Name the blood parasite species.
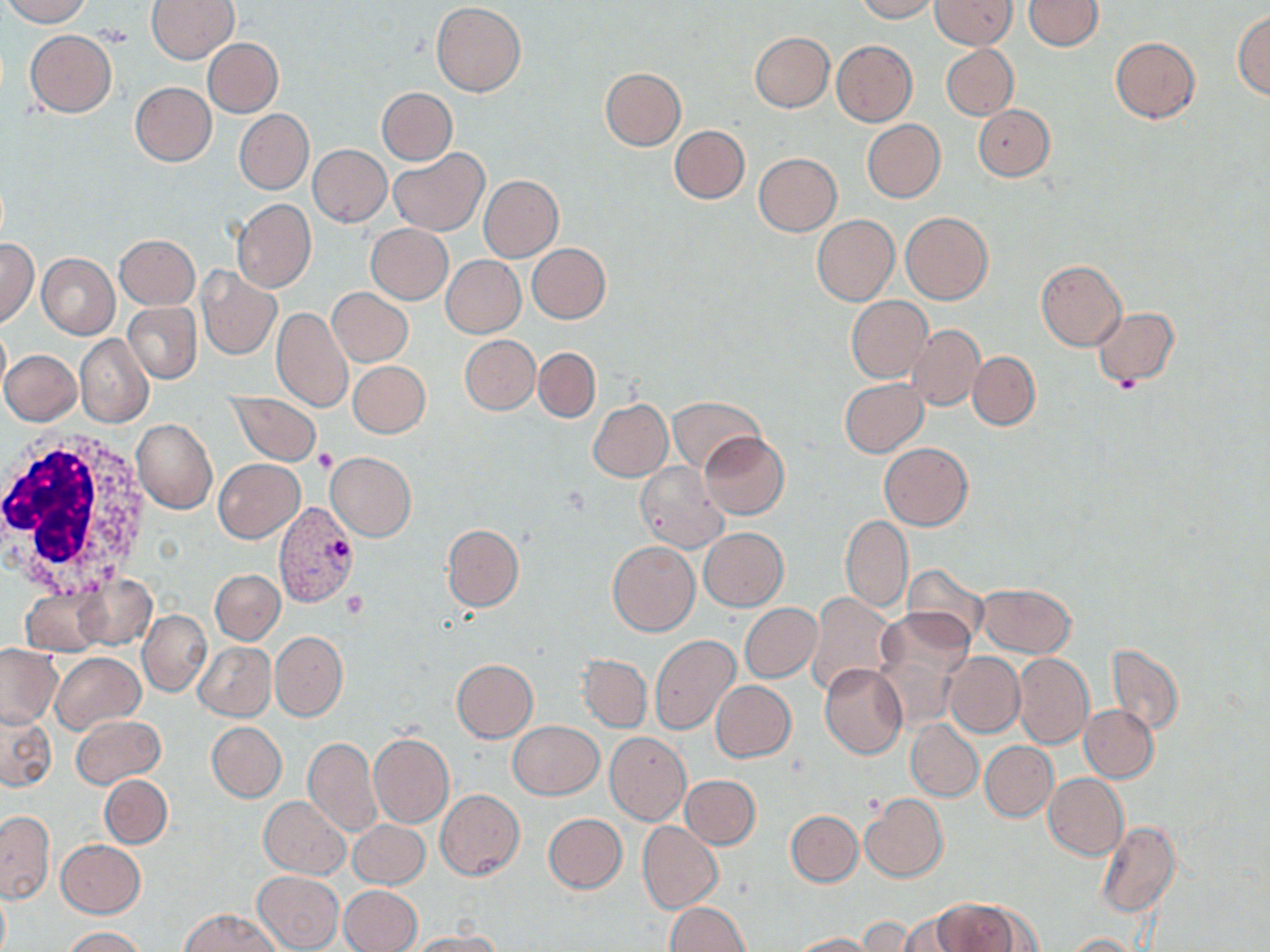

Plasmodium vivax.

Approximate bounding boxes as named x1/y1/x2/y2 corners in pixels. Platelet locations: (x1=312, y1=449, x2=337, y2=473), (x1=342, y1=590, x2=367, y2=620). Plasmodium vivax-infected red blood cell locations: (x1=273, y1=501, x2=356, y2=608). White blood cell locations: (x1=0, y1=428, x2=157, y2=598). Uninfected red blood cell locations: (x1=1, y1=0, x2=92, y2=26), (x1=147, y1=0, x2=239, y2=64), (x1=854, y1=0, x2=937, y2=22), (x1=930, y1=0, x2=1015, y2=49), (x1=1024, y1=0, x2=1104, y2=51), (x1=432, y1=2, x2=525, y2=96), (x1=1232, y1=9, x2=1270, y2=99), (x1=24, y1=29, x2=116, y2=117), (x1=749, y1=32, x2=833, y2=113), (x1=1110, y1=36, x2=1200, y2=122), (x1=202, y1=38, x2=283, y2=117), (x1=831, y1=40, x2=917, y2=126), (x1=941, y1=45, x2=1018, y2=120), (x1=599, y1=67, x2=686, y2=151), (x1=130, y1=82, x2=216, y2=166), (x1=378, y1=88, x2=456, y2=165), (x1=973, y1=104, x2=1054, y2=181), (x1=233, y1=109, x2=313, y2=194), (x1=862, y1=119, x2=945, y2=203), (x1=669, y1=124, x2=750, y2=204), (x1=308, y1=144, x2=392, y2=227), (x1=388, y1=148, x2=489, y2=235), (x1=753, y1=153, x2=841, y2=236), (x1=479, y1=176, x2=562, y2=261), (x1=232, y1=198, x2=316, y2=293), (x1=900, y1=212, x2=993, y2=305), (x1=812, y1=214, x2=899, y2=306), (x1=366, y1=224, x2=453, y2=304), (x1=115, y1=234, x2=199, y2=309), (x1=0, y1=238, x2=39, y2=327), (x1=527, y1=243, x2=611, y2=324), (x1=37, y1=253, x2=120, y2=338), (x1=441, y1=255, x2=525, y2=338), (x1=1037, y1=259, x2=1126, y2=351), (x1=196, y1=267, x2=281, y2=359), (x1=328, y1=287, x2=413, y2=367), (x1=846, y1=296, x2=933, y2=384), (x1=123, y1=302, x2=200, y2=382), (x1=272, y1=307, x2=352, y2=412), (x1=1091, y1=308, x2=1179, y2=388), (x1=909, y1=324, x2=985, y2=411), (x1=0, y1=327, x2=11, y2=398), (x1=75, y1=335, x2=153, y2=426), (x1=460, y1=335, x2=540, y2=414), (x1=534, y1=347, x2=600, y2=422), (x1=0, y1=349, x2=82, y2=425), (x1=968, y1=352, x2=1039, y2=430), (x1=348, y1=360, x2=430, y2=438), (x1=840, y1=379, x2=928, y2=456), (x1=229, y1=391, x2=320, y2=465), (x1=668, y1=396, x2=765, y2=474), (x1=588, y1=399, x2=672, y2=482), (x1=132, y1=417, x2=217, y2=514), (x1=699, y1=432, x2=789, y2=518), (x1=879, y1=443, x2=972, y2=530), (x1=326, y1=452, x2=416, y2=541), (x1=213, y1=458, x2=303, y2=543), (x1=635, y1=462, x2=728, y2=551), (x1=841, y1=516, x2=913, y2=612), (x1=441, y1=524, x2=524, y2=610), (x1=699, y1=528, x2=787, y2=610), (x1=608, y1=541, x2=699, y2=636), (x1=902, y1=564, x2=989, y2=647), (x1=211, y1=569, x2=284, y2=645), (x1=72, y1=573, x2=159, y2=652), (x1=975, y1=583, x2=1076, y2=656), (x1=21, y1=588, x2=108, y2=656), (x1=805, y1=593, x2=895, y2=695), (x1=740, y1=603, x2=821, y2=682), (x1=876, y1=605, x2=976, y2=697), (x1=139, y1=611, x2=210, y2=696), (x1=271, y1=631, x2=348, y2=720), (x1=650, y1=635, x2=741, y2=736), (x1=194, y1=641, x2=275, y2=722), (x1=1107, y1=642, x2=1184, y2=736), (x1=0, y1=644, x2=62, y2=728), (x1=943, y1=651, x2=1025, y2=738), (x1=51, y1=652, x2=145, y2=736), (x1=1013, y1=652, x2=1093, y2=751), (x1=579, y1=654, x2=651, y2=730), (x1=452, y1=659, x2=538, y2=741), (x1=819, y1=662, x2=907, y2=759), (x1=709, y1=680, x2=797, y2=762), (x1=1079, y1=704, x2=1158, y2=782), (x1=2, y1=712, x2=57, y2=791), (x1=71, y1=715, x2=166, y2=787), (x1=906, y1=719, x2=983, y2=801), (x1=509, y1=721, x2=603, y2=799), (x1=206, y1=722, x2=287, y2=802), (x1=367, y1=732, x2=453, y2=828), (x1=605, y1=733, x2=691, y2=825), (x1=303, y1=737, x2=381, y2=837), (x1=980, y1=741, x2=1058, y2=820), (x1=1042, y1=773, x2=1128, y2=859), (x1=100, y1=774, x2=172, y2=849), (x1=680, y1=774, x2=761, y2=848), (x1=436, y1=789, x2=524, y2=881), (x1=860, y1=795, x2=947, y2=882), (x1=260, y1=797, x2=349, y2=879), (x1=786, y1=810, x2=863, y2=886), (x1=0, y1=812, x2=53, y2=902), (x1=543, y1=813, x2=627, y2=893), (x1=349, y1=820, x2=429, y2=887), (x1=1096, y1=821, x2=1180, y2=918), (x1=638, y1=822, x2=722, y2=913), (x1=56, y1=839, x2=145, y2=918), (x1=252, y1=871, x2=343, y2=952), (x1=339, y1=884, x2=422, y2=952), (x1=0, y1=888, x2=10, y2=952), (x1=934, y1=898, x2=1037, y2=951), (x1=665, y1=901, x2=750, y2=951), (x1=180, y1=908, x2=280, y2=952), (x1=888, y1=911, x2=975, y2=952), (x1=854, y1=917, x2=940, y2=950), (x1=61, y1=926, x2=145, y2=952), (x1=403, y1=931, x2=504, y2=951), (x1=787, y1=933, x2=879, y2=952), (x1=1064, y1=933, x2=1144, y2=952). Captured at 1000x magnification. Optical microscopy. Thin blood smear. One field of a larger specimen. May-Grünwald-Giemsa-stained preparation. Image is 1270×952 pixels.